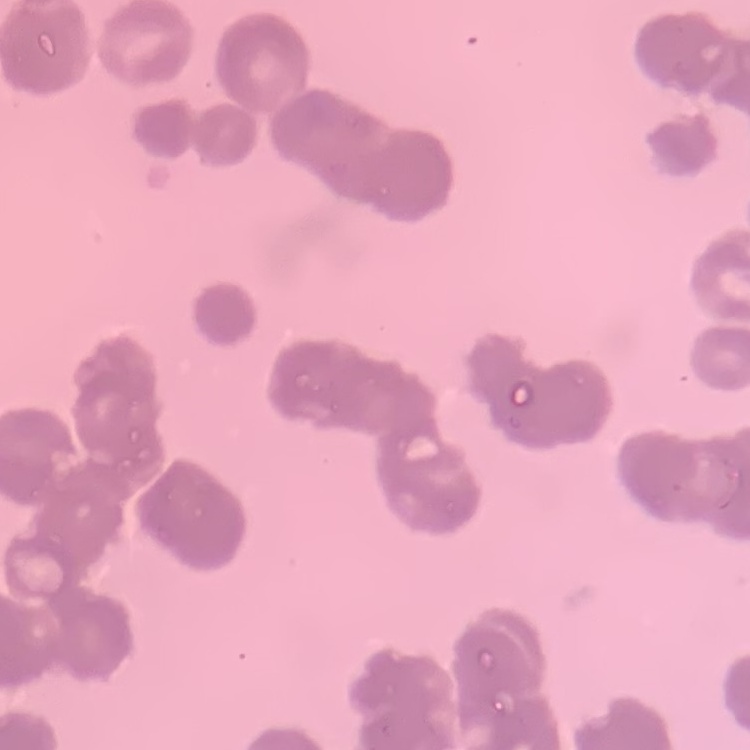
The red blood cells show rouleaux formation. Stained with either Field's or Giemsa. Square crop of a larger photomicrograph. Thin blood film.